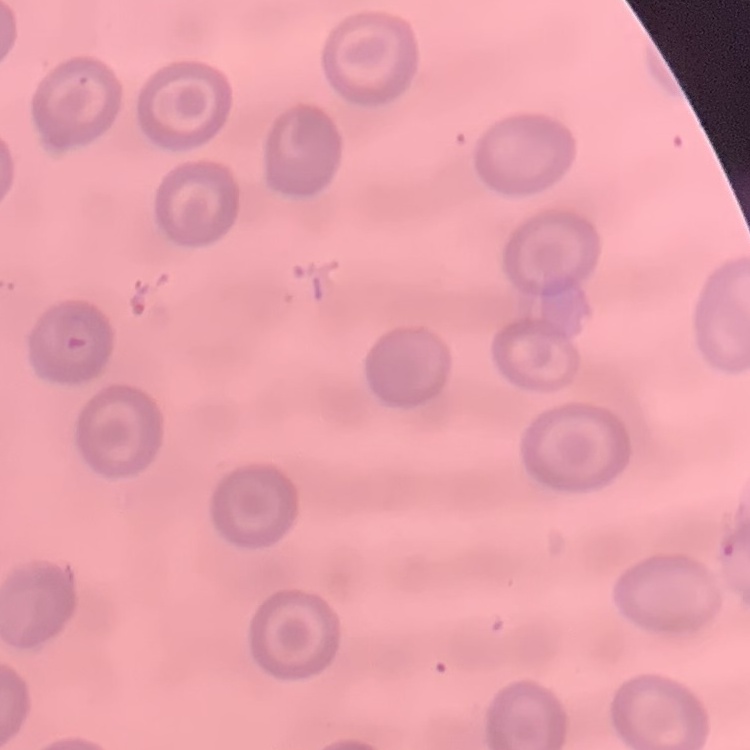

{
  "red_blood_cell_morphology": "no rouleaux formation",
  "preparation": "thin peripheral smear",
  "image_type": "square crop of a larger photomicrograph",
  "stain": "Field's or Giemsa"
}